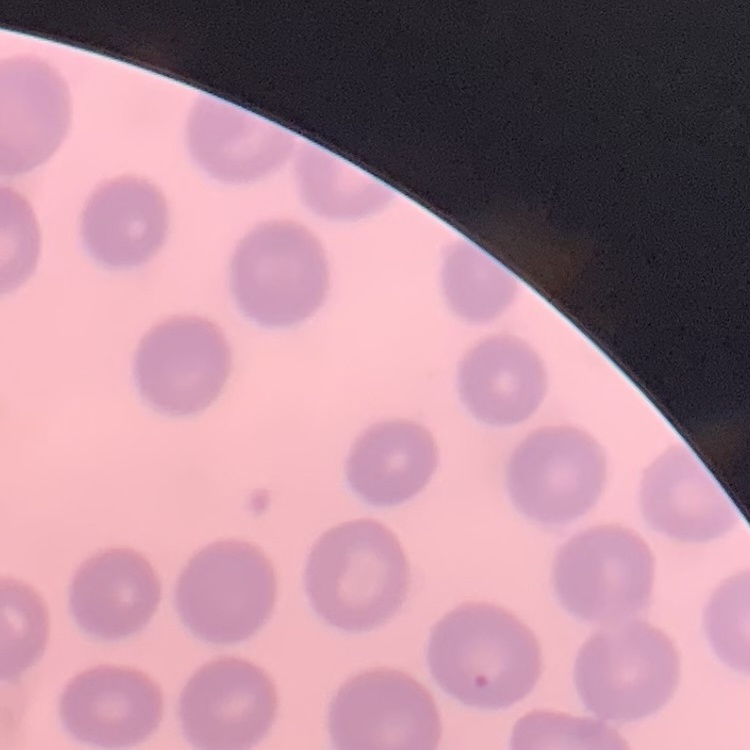

The erythrocytes exhibit no rouleaux formation. Thin blood smear. Stained with either Field's or Giemsa. One tile cut from a larger photomicrograph.